Comment on the background quality.
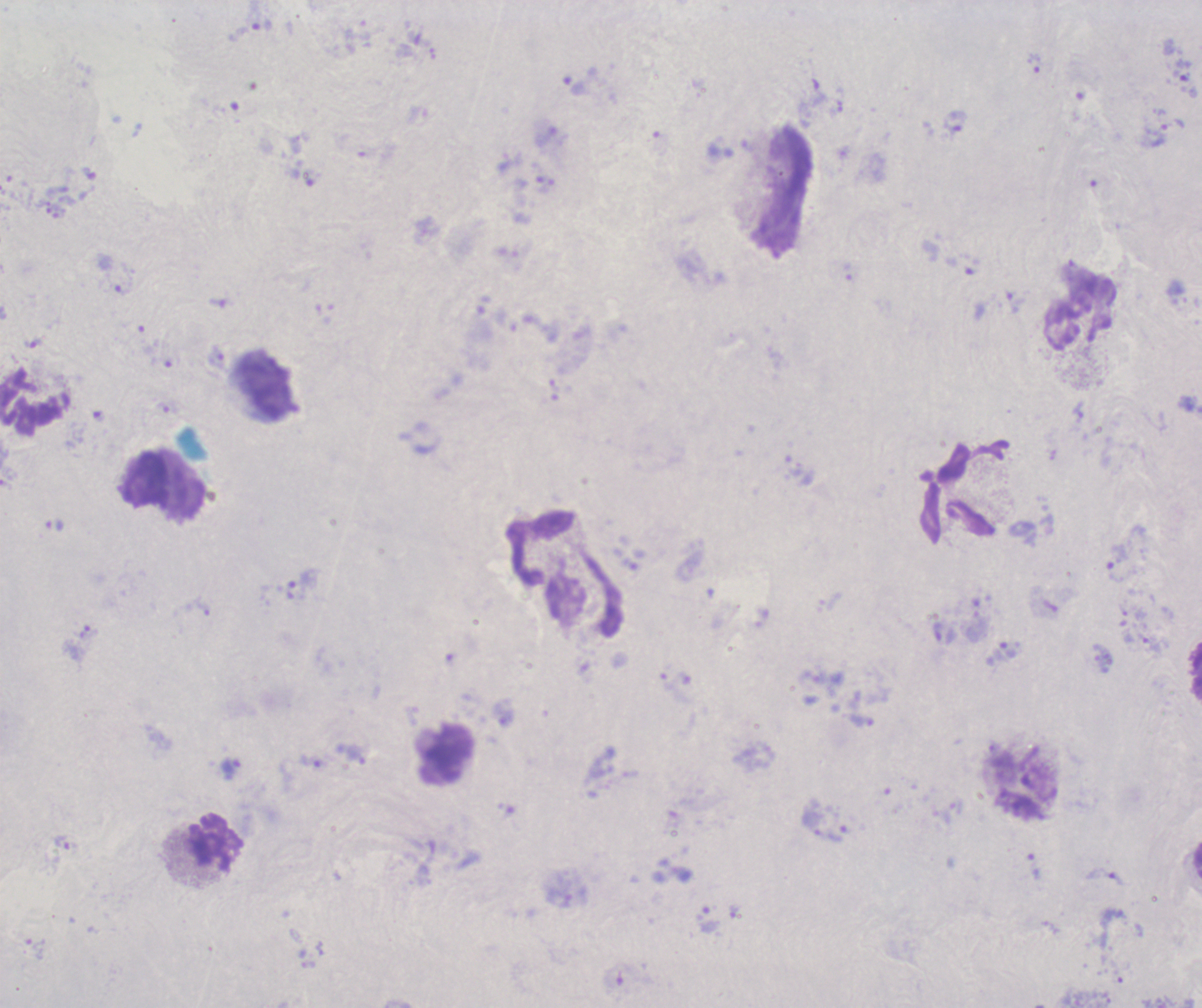
Poor.

Approximate centers as [x, y] in pixels.
Summary:
  - Leukocyte locations: [266, 387], [31, 405], [147, 482], [446, 753], [1025, 786], [215, 842]
  - Trophozoite locations: [262, 25], [1034, 63], [574, 85], [956, 121], [1156, 135], [1015, 302], [216, 359], [54, 525], [1116, 563], [302, 581], [203, 608], [230, 766], [62, 841], [1034, 867], [1105, 877]
  - Magnification: 100x
  - Stain: Romanowsky
  - Context: previously used in a real diagnosis
  - Image size: 1202×1008 pixels
  - Field of view: one from this slide
  - Result: Plasmodium parasites identified
  - Preparation: thick smear of blood